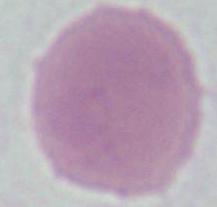
{
  "modality": "photomicrograph",
  "magnification": "1000x",
  "identification": "erythrocyte"
}